Assess this cell for malaria.
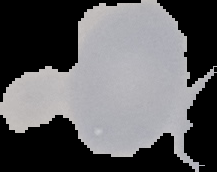

It is uninfected.

Summary:
  - Preparation: thin blood film
  - Image type: segmented cell region with the area outside set to black
  - Image size: 217×172 pixels